Name the parasite shown.
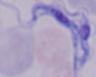
This is a trypanosome.

Captured at 1000x magnification. Photomicrograph.